Classify this cell by malaria status.
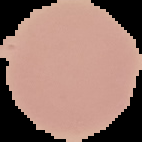
It is uninfected.

{
  "preparation": "thin blood film",
  "image_size": "142×142 pixels",
  "image_type": "segmented cell region with the area outside set to black"
}